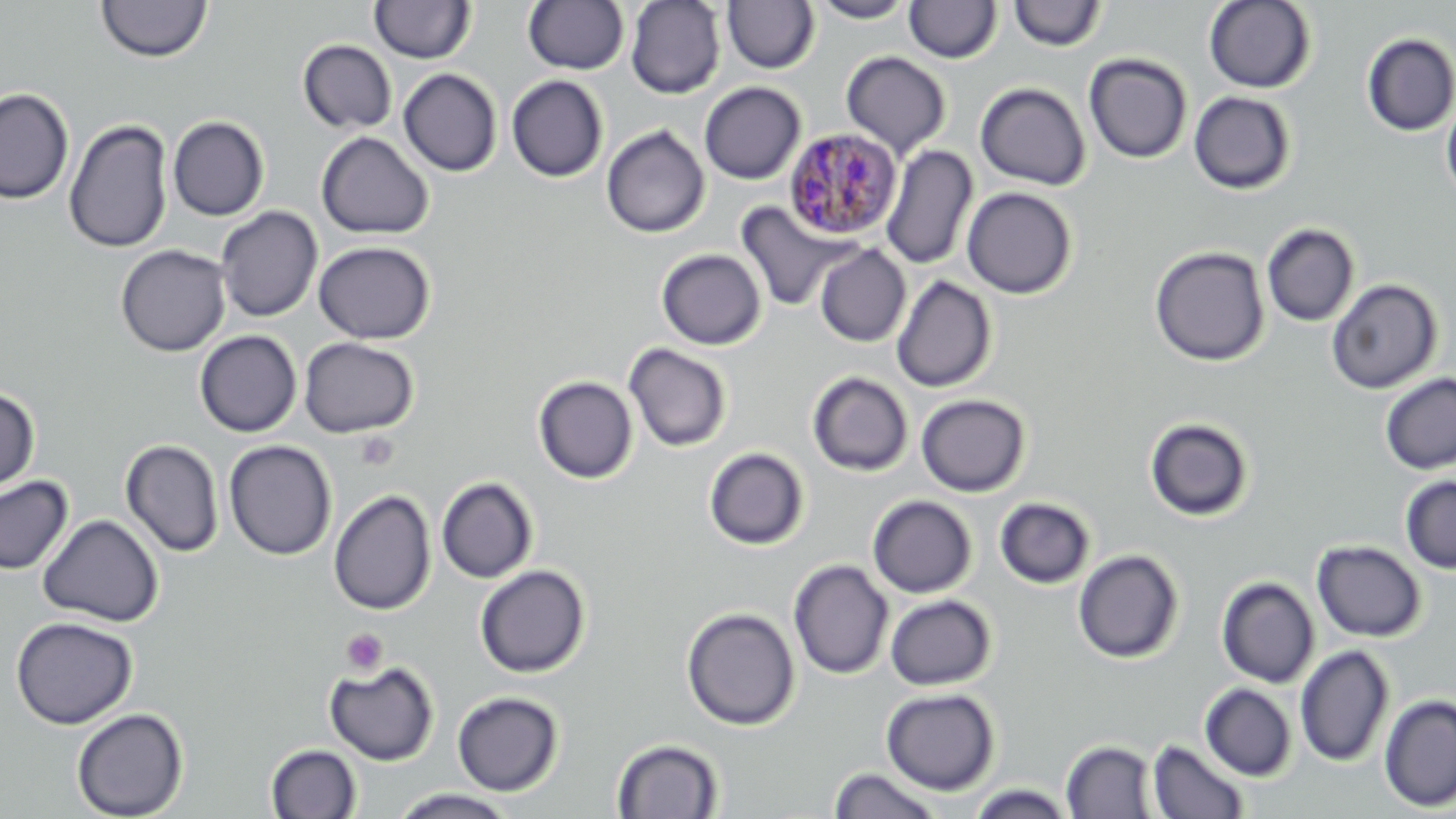

Summary:
  - Coordinate format: approximate bounding boxes as (x1, y1, x2, y2) in pixels
  - Plasmodium malariae-infected red blood cell locations: (783, 128, 903, 240)
  - Platelet locations: (355, 430, 399, 471), (341, 628, 388, 675)
  - Uninfected red blood cell locations: (97, 0, 213, 63), (370, 0, 476, 64), (523, 0, 629, 75), (625, 0, 726, 98), (722, 1, 819, 74), (809, 1, 916, 23), (904, 1, 1001, 63), (1007, 1, 1107, 52), (1203, 1, 1317, 93), (1361, 33, 1456, 136), (298, 39, 397, 133), (841, 51, 952, 159), (1084, 53, 1193, 164), (398, 68, 502, 177), (506, 75, 609, 182), (699, 82, 805, 184), (975, 82, 1091, 191), (0, 87, 74, 204), (1188, 91, 1296, 195), (1441, 97, 1456, 201), (167, 116, 270, 221), (64, 119, 175, 253), (601, 125, 710, 238), (316, 131, 434, 239), (880, 145, 978, 270), (961, 186, 1078, 299), (737, 202, 856, 312), (216, 206, 323, 323), (1262, 223, 1360, 327), (313, 241, 436, 344), (115, 244, 231, 357), (814, 245, 911, 347), (1149, 245, 1270, 367), (656, 249, 767, 350), (892, 275, 997, 393), (1326, 279, 1442, 394), (194, 330, 303, 437), (299, 337, 419, 438), (623, 343, 732, 452), (807, 372, 913, 477), (1380, 373, 1456, 475), (533, 375, 638, 484), (0, 387, 40, 495), (916, 394, 1030, 497), (1144, 417, 1254, 522), (120, 439, 224, 558), (223, 440, 337, 560), (704, 447, 809, 550), (0, 475, 74, 575), (1400, 475, 1456, 574), (436, 477, 538, 583), (328, 489, 436, 616), (867, 495, 977, 598), (994, 497, 1095, 589), (38, 514, 164, 627), (1312, 540, 1426, 642), (1073, 549, 1184, 663), (788, 559, 894, 679), (475, 565, 591, 678), (1217, 577, 1319, 688), (885, 595, 997, 690), (681, 607, 801, 731), (11, 616, 138, 729), (1295, 645, 1395, 767), (324, 661, 439, 765), (1200, 683, 1297, 780), (881, 687, 1000, 795), (452, 691, 563, 796), (1379, 694, 1456, 811), (71, 707, 189, 819), (611, 738, 725, 818), (1147, 739, 1250, 819), (1061, 740, 1159, 818), (265, 744, 362, 819), (828, 767, 946, 818), (964, 784, 1078, 819), (386, 789, 522, 819)
  - Slide-level diagnosis: Plasmodium malariae
  - Stain: May-Grünwald-Giemsa
  - Image size: 1456×819 pixels
  - Field of view: single
  - Magnification: 1000x
  - Modality: light microscopy
  - Preparation: thin blood film